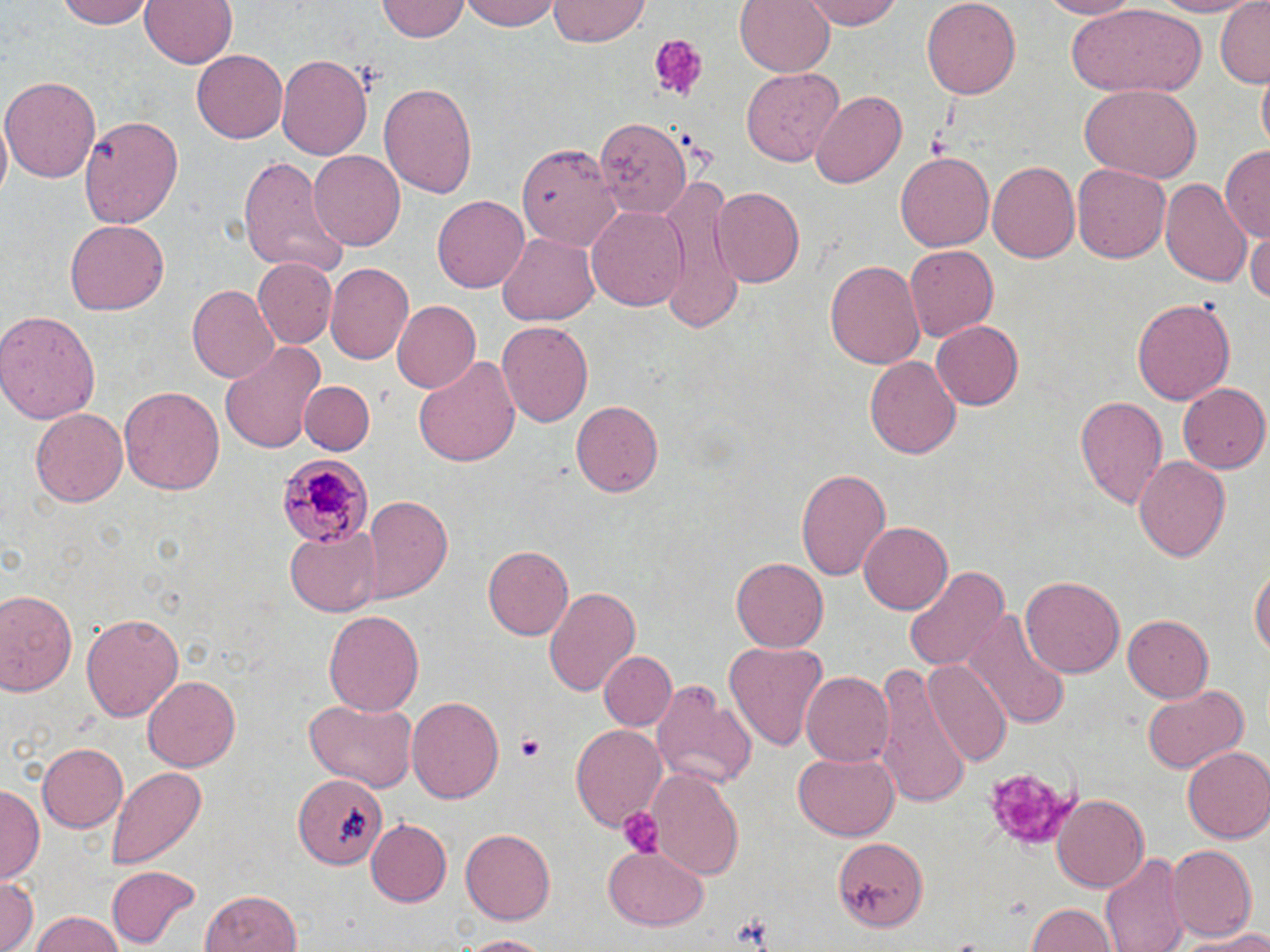 Approximate bounding boxes as named x1/y1/x2/y2 corners in pixels. Platelet locations: (x1=648, y1=33, x2=705, y2=101), (x1=514, y1=733, x2=547, y2=762), (x1=981, y1=762, x2=1076, y2=850), (x1=619, y1=807, x2=662, y2=858). Uninfected red blood cell locations: (x1=59, y1=0, x2=156, y2=28), (x1=139, y1=0, x2=238, y2=69), (x1=461, y1=0, x2=560, y2=32), (x1=735, y1=0, x2=834, y2=75), (x1=803, y1=0, x2=903, y2=29), (x1=1034, y1=0, x2=1143, y2=19), (x1=1139, y1=0, x2=1262, y2=15), (x1=1216, y1=0, x2=1269, y2=86), (x1=377, y1=1, x2=469, y2=43), (x1=546, y1=1, x2=651, y2=46), (x1=920, y1=1, x2=1023, y2=98), (x1=1064, y1=5, x2=1209, y2=94), (x1=192, y1=50, x2=289, y2=143), (x1=275, y1=51, x2=374, y2=163), (x1=740, y1=67, x2=843, y2=166), (x1=1254, y1=71, x2=1269, y2=149), (x1=3, y1=74, x2=101, y2=183), (x1=379, y1=81, x2=478, y2=197), (x1=1079, y1=83, x2=1202, y2=183), (x1=812, y1=89, x2=908, y2=187), (x1=592, y1=112, x2=693, y2=217), (x1=80, y1=113, x2=182, y2=231), (x1=516, y1=142, x2=623, y2=255), (x1=1221, y1=146, x2=1269, y2=242), (x1=308, y1=150, x2=405, y2=252), (x1=895, y1=151, x2=994, y2=253), (x1=236, y1=153, x2=346, y2=276), (x1=989, y1=161, x2=1081, y2=265), (x1=1072, y1=162, x2=1171, y2=264), (x1=1161, y1=176, x2=1254, y2=287), (x1=659, y1=178, x2=743, y2=319), (x1=710, y1=187, x2=805, y2=287), (x1=432, y1=194, x2=529, y2=292), (x1=586, y1=205, x2=689, y2=310), (x1=66, y1=217, x2=169, y2=313), (x1=1246, y1=228, x2=1270, y2=307), (x1=495, y1=232, x2=597, y2=327), (x1=904, y1=244, x2=1001, y2=341), (x1=824, y1=258, x2=925, y2=369), (x1=252, y1=259, x2=336, y2=347), (x1=325, y1=263, x2=414, y2=367), (x1=186, y1=284, x2=278, y2=382), (x1=391, y1=297, x2=481, y2=391), (x1=1131, y1=297, x2=1234, y2=405), (x1=0, y1=309, x2=102, y2=425), (x1=498, y1=319, x2=594, y2=430), (x1=931, y1=319, x2=1024, y2=407), (x1=219, y1=340, x2=327, y2=454), (x1=866, y1=355, x2=961, y2=461), (x1=413, y1=357, x2=521, y2=469), (x1=301, y1=380, x2=373, y2=455), (x1=120, y1=384, x2=225, y2=498), (x1=1178, y1=384, x2=1270, y2=473), (x1=1074, y1=394, x2=1169, y2=512), (x1=571, y1=400, x2=664, y2=497), (x1=30, y1=409, x2=127, y2=506), (x1=1133, y1=456, x2=1230, y2=563), (x1=795, y1=466, x2=892, y2=580), (x1=360, y1=494, x2=454, y2=605), (x1=858, y1=520, x2=954, y2=614), (x1=285, y1=528, x2=380, y2=616), (x1=483, y1=543, x2=574, y2=640), (x1=732, y1=555, x2=830, y2=652), (x1=1251, y1=562, x2=1269, y2=668), (x1=903, y1=563, x2=1010, y2=673), (x1=1021, y1=576, x2=1124, y2=680), (x1=543, y1=582, x2=641, y2=697), (x1=0, y1=589, x2=81, y2=698), (x1=323, y1=609, x2=424, y2=719), (x1=80, y1=613, x2=184, y2=720), (x1=969, y1=613, x2=1071, y2=729), (x1=1121, y1=615, x2=1212, y2=704), (x1=724, y1=640, x2=829, y2=751), (x1=600, y1=650, x2=677, y2=731), (x1=919, y1=659, x2=1012, y2=770), (x1=873, y1=663, x2=974, y2=806), (x1=800, y1=672, x2=893, y2=768), (x1=143, y1=675, x2=240, y2=772), (x1=650, y1=678, x2=758, y2=791), (x1=1141, y1=686, x2=1249, y2=773), (x1=405, y1=695, x2=503, y2=805), (x1=301, y1=697, x2=420, y2=793), (x1=570, y1=725, x2=668, y2=831), (x1=37, y1=742, x2=129, y2=832), (x1=1182, y1=746, x2=1270, y2=844), (x1=792, y1=751, x2=900, y2=841), (x1=103, y1=765, x2=207, y2=871), (x1=649, y1=770, x2=744, y2=879), (x1=295, y1=772, x2=385, y2=872), (x1=1, y1=786, x2=41, y2=883), (x1=1052, y1=793, x2=1151, y2=891), (x1=366, y1=819, x2=452, y2=905), (x1=460, y1=828, x2=556, y2=924), (x1=834, y1=836, x2=931, y2=933), (x1=1166, y1=844, x2=1258, y2=941), (x1=603, y1=846, x2=710, y2=932), (x1=1100, y1=852, x2=1189, y2=952), (x1=106, y1=866, x2=202, y2=948), (x1=0, y1=874, x2=38, y2=952), (x1=197, y1=889, x2=304, y2=952), (x1=1024, y1=903, x2=1116, y2=952), (x1=29, y1=910, x2=125, y2=952), (x1=1181, y1=930, x2=1270, y2=950), (x1=452, y1=933, x2=555, y2=950). Plasmodium malariae-infected red blood cell locations: (x1=273, y1=452, x2=375, y2=549). Slide-level diagnosis: Plasmodium malariae. May-Grünwald-Giemsa-stained preparation. Thin blood film. Single field of view. Light microscopy. Image is 1270×952 pixels. 1000x magnification.